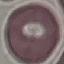

result = negative for malaria parasites
image type = automatically extracted cell patch, resized to 64 × 64 pixels
stain = Giemsa
capture = smartphone through the microscope eyepiece
preparation = thin smear